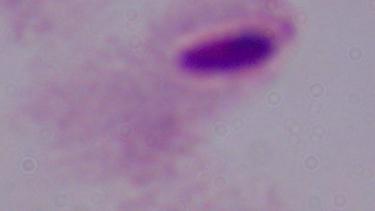

magnification: 1000x
identification: trichomonad
modality: photomicrograph